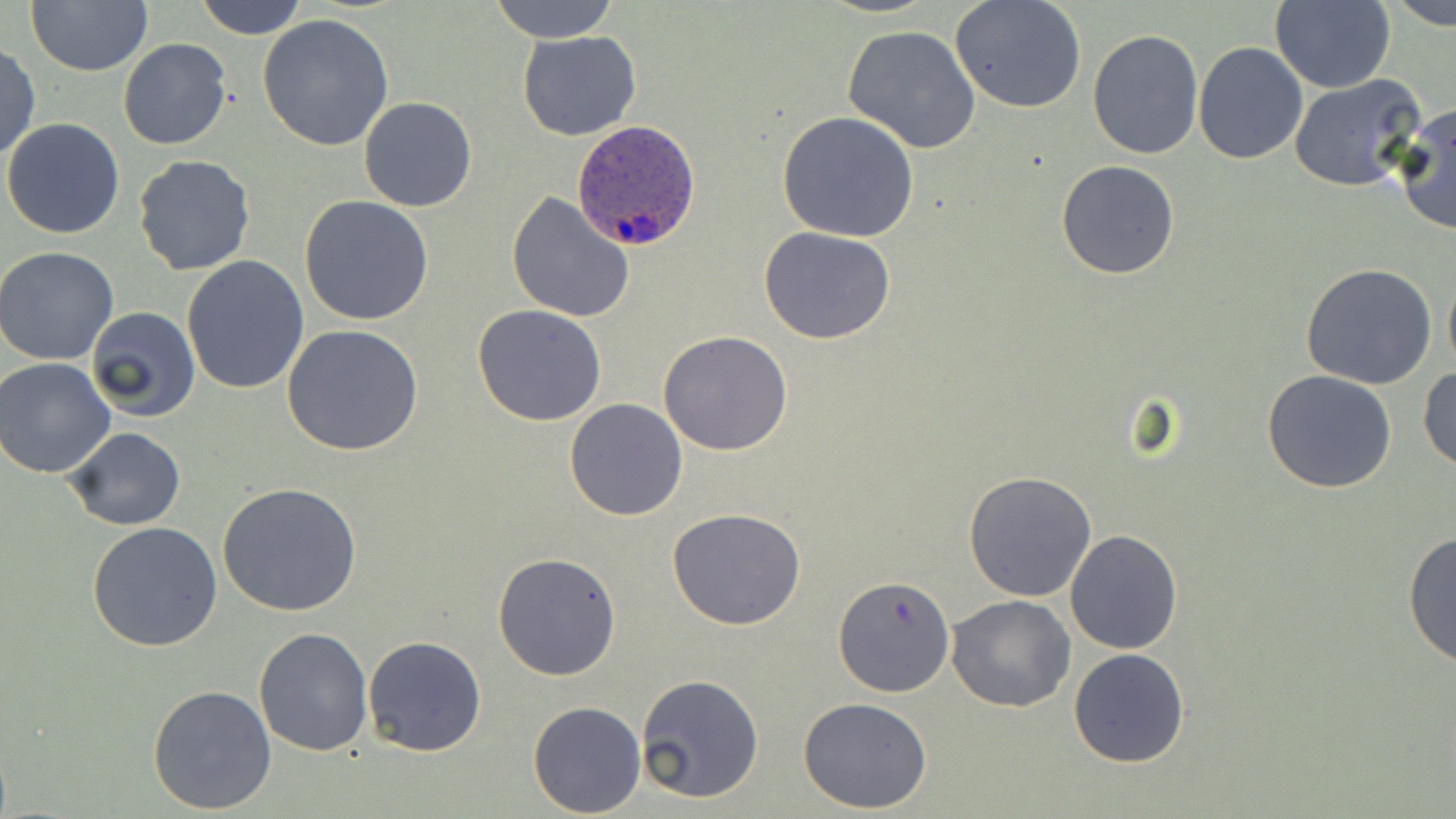
Approximate bounding boxes as (x1,y1)-(x2,y2) corner pairs in pixels. Plasmodium ovale-infected red blood cell locations: (571,119)-(702,251). Uninfected red blood cell locations: (193,0)-(307,38), (489,0)-(620,42), (1387,0)-(1455,28), (27,1)-(153,77), (949,1)-(1088,115), (1268,1)-(1396,92), (257,11)-(395,151), (841,24)-(983,154), (1086,28)-(1204,160), (517,30)-(642,141), (118,37)-(232,150), (1192,42)-(1308,164), (1,44)-(40,163), (1287,74)-(1428,192), (358,97)-(476,211), (1393,103)-(1456,237), (776,112)-(920,243), (2,118)-(126,239), (133,155)-(255,276), (1056,160)-(1180,279), (505,191)-(636,323), (299,195)-(434,325), (757,227)-(897,346), (0,246)-(122,365), (181,255)-(310,395), (1301,262)-(1438,390), (1443,264)-(1456,378), (472,304)-(607,426), (83,306)-(200,424), (281,325)-(424,456), (659,330)-(793,457), (0,356)-(119,477), (1418,365)-(1456,474), (1262,370)-(1397,494), (564,398)-(688,520), (64,427)-(186,531), (964,470)-(1096,601), (219,483)-(363,617), (666,507)-(808,629), (85,520)-(225,652), (1064,529)-(1182,654), (1402,531)-(1455,668), (493,552)-(622,680), (836,576)-(953,695), (946,595)-(1076,712), (254,627)-(374,756), (363,635)-(487,756), (1068,646)-(1192,767), (635,672)-(765,804), (146,682)-(277,815), (797,696)-(933,813), (528,701)-(645,816). Slide-level diagnosis: Plasmodium ovale. Single field of view. Optical microscopy. 1000x magnification. Image is 1456×819 pixels. May-Grünwald-Giemsa-stained preparation. Thin blood film.